Point out each malaria parasite.
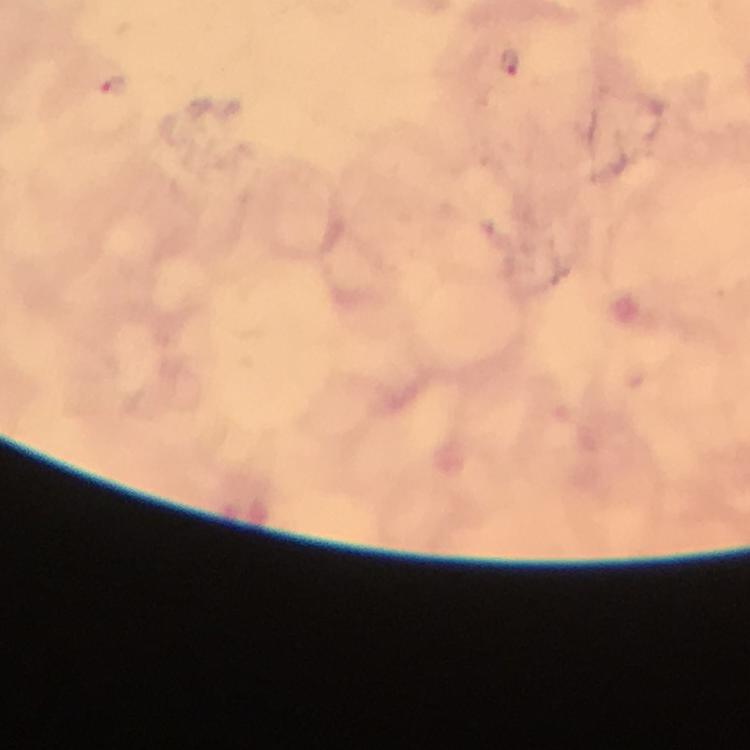

Approximate centers as {x, y} in pixels.
Malaria parasites: {508, 61}, {117, 86}.

{
  "capture": "smartphone photograph through a microscope",
  "context": "from a malaria diagnostic workup",
  "stain": "Giemsa",
  "immersion_oil": "used",
  "magnification": "100x",
  "image_size": "750×750 pixels",
  "preparation": "thick blood film",
  "cropped_from": "one field of view"
}